Locate every blood parasite and identify its species.
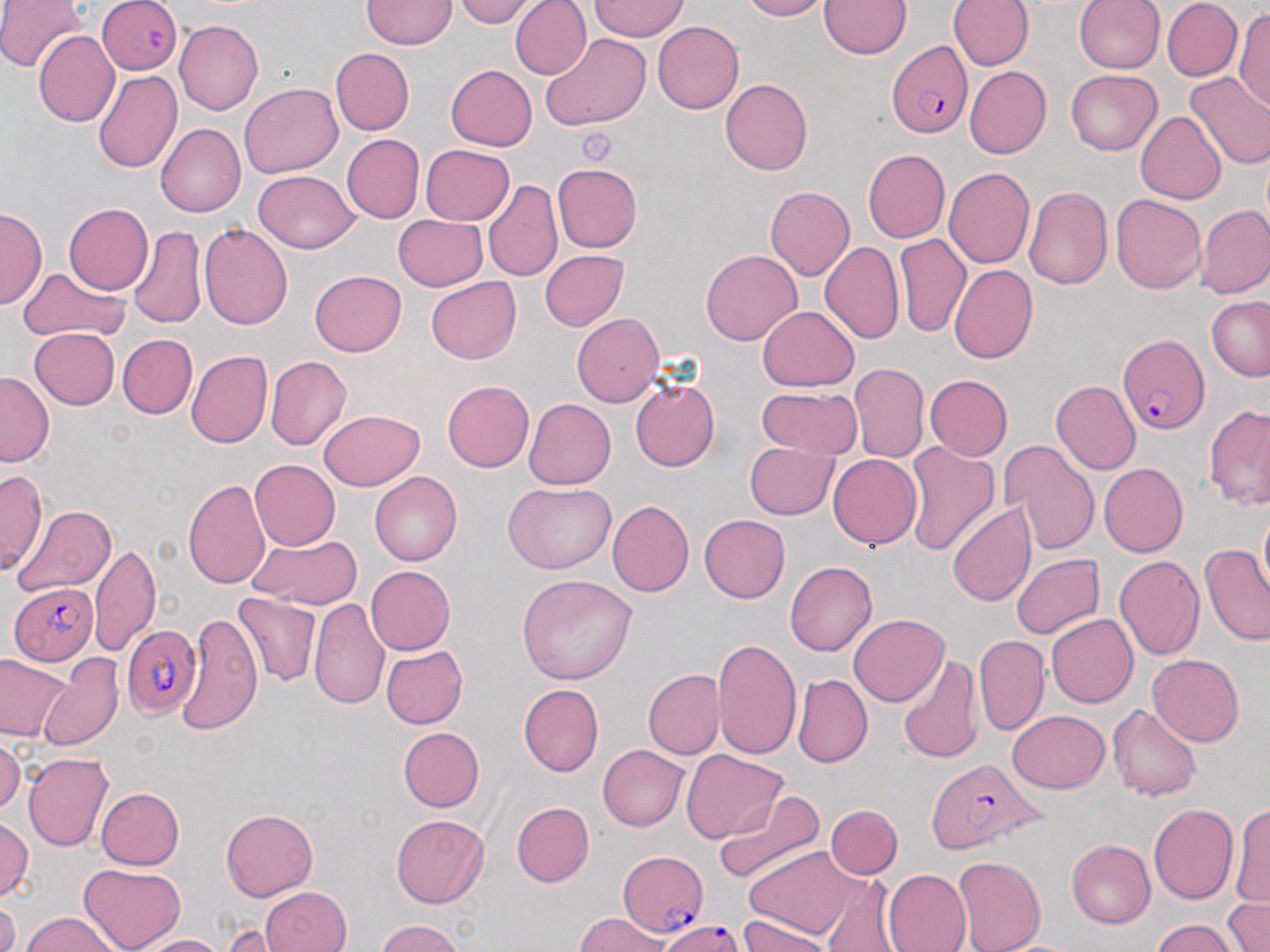
Approximate bounding boxes as (x1,y1)-(x2,y2) corner pairs in pixels.
Plasmodium falciparum-infected red blood cells: (100,0)-(182,74), (887,40)-(972,138), (1118,334)-(1209,435), (8,582)-(97,665), (120,623)-(200,719), (926,756)-(1046,854), (617,851)-(708,938), (659,918)-(744,952).
No Plasmodium ovale, Plasmodium malariae, Plasmodium vivax, Babesia divergens, or Trypanosoma brucei observed.

Summary:
  - Platelet locations: (576,126)-(620,167)
  - Uninfected red blood cell locations: (0,0)-(85,73), (454,0)-(543,27), (510,0)-(591,80), (738,0)-(830,20), (820,0)-(911,58), (948,0)-(1033,71), (1073,0)-(1165,74), (1162,0)-(1242,82), (362,1)-(455,49), (591,1)-(690,41), (1234,6)-(1270,113), (174,20)-(264,116), (652,20)-(744,114), (34,30)-(119,128), (540,33)-(652,133), (330,47)-(414,136), (445,64)-(537,151), (964,66)-(1051,159), (1065,69)-(1162,155), (93,70)-(182,173), (1185,72)-(1270,170), (720,78)-(812,176), (240,83)-(343,178), (1135,111)-(1226,204), (155,123)-(246,218), (341,134)-(425,223), (421,145)-(514,225), (862,148)-(951,243), (552,162)-(643,252), (944,167)-(1035,268), (251,170)-(360,254), (482,178)-(562,282), (1024,185)-(1113,291), (764,186)-(855,280), (1110,194)-(1207,294), (63,203)-(154,295), (1195,204)-(1270,298), (0,206)-(45,309), (393,214)-(487,291), (198,222)-(294,330), (128,226)-(207,330), (895,232)-(970,337), (819,242)-(904,344), (894,247)-(1029,350), (700,248)-(802,346), (539,250)-(629,331), (948,264)-(1038,364), (18,267)-(127,341), (309,270)-(407,356), (425,277)-(521,365), (1206,296)-(1270,381), (757,306)-(859,391), (571,313)-(664,408), (29,328)-(120,410), (117,334)-(196,419), (186,351)-(272,449), (265,355)-(352,450), (850,362)-(929,462), (0,370)-(53,467), (924,374)-(1012,460), (442,380)-(535,472), (629,380)-(720,472), (1051,380)-(1141,475), (756,386)-(863,458), (523,398)-(616,488), (1204,403)-(1270,511), (317,409)-(424,491), (998,439)-(1100,555), (901,440)-(999,557), (745,442)-(838,519), (828,455)-(922,550), (249,459)-(341,550), (1099,462)-(1188,558), (1,470)-(48,574), (370,471)-(462,566), (183,477)-(272,591), (503,481)-(615,574), (606,500)-(695,598), (946,501)-(1035,605), (12,503)-(117,596), (1258,507)-(1270,602), (699,514)-(790,603), (248,534)-(361,608), (89,543)-(160,657), (1199,543)-(1270,645), (1010,554)-(1105,639), (1114,554)-(1205,659), (784,559)-(877,657), (365,565)-(455,655), (516,574)-(639,685), (233,593)-(321,686), (309,599)-(390,709), (176,610)-(261,735), (848,614)-(947,706), (1046,614)-(1138,708), (974,635)-(1050,735), (712,636)-(801,762), (381,645)-(467,729), (386,645)-(474,811), (37,653)-(124,751), (898,653)-(984,766), (1148,653)-(1244,747), (0,654)-(73,741), (643,669)-(724,759), (793,674)-(872,768), (518,683)-(603,777), (1108,704)-(1201,802), (1005,710)-(1109,793), (398,727)-(485,812), (0,736)-(25,813), (597,744)-(689,831), (682,750)-(788,843), (22,752)-(114,851), (96,787)-(185,869), (714,789)-(826,887), (510,802)-(593,887), (1229,802)-(1270,910), (826,804)-(902,878), (1148,804)-(1239,904), (221,809)-(318,901), (391,815)-(488,907), (1,816)-(33,901), (1066,839)-(1155,929), (746,845)-(866,940), (952,855)-(1046,952), (78,864)-(187,952), (883,869)-(972,952), (820,874)-(902,951), (261,886)-(350,952), (1222,896)-(1269,952), (0,897)-(19,952), (21,912)-(121,951), (576,912)-(673,951), (738,916)-(837,951), (374,919)-(468,952), (1149,919)-(1240,952), (221,921)-(299,950), (131,934)-(227,952)
  - Slide-level diagnosis: Plasmodium falciparum
  - Stain: May-Grünwald-Giemsa
  - Image size: 1270×952 pixels
  - Field of view: one of a larger specimen
  - Modality: optical microscopy
  - Magnification: 1000x
  - Preparation: thin blood smear